Classify this cell by malaria status.
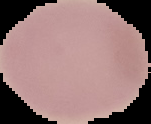

It is uninfected.

preparation = thin blood film
image type = segmented cell region on a black background
image size = 151×124 pixels